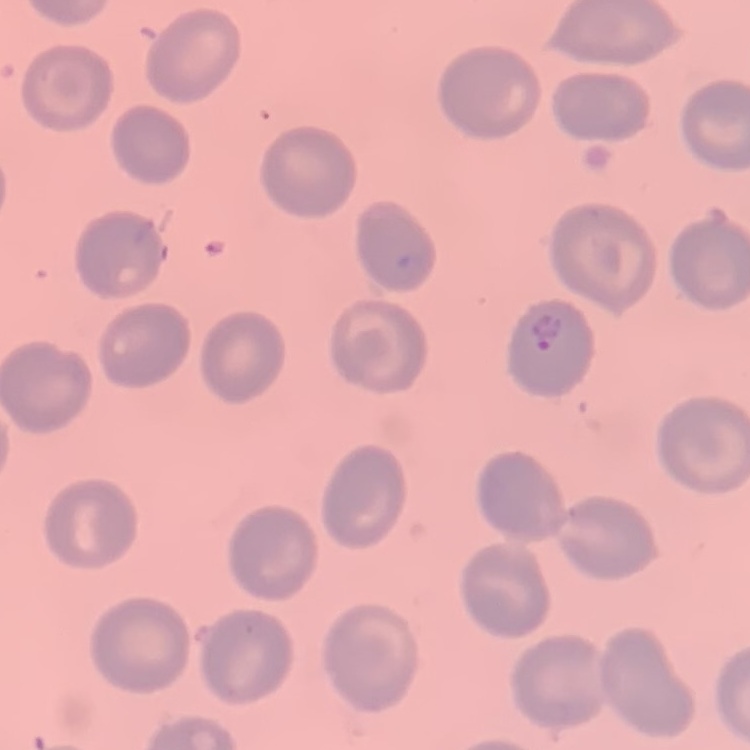
erythrocyte morphology = no rouleaux formation
stain = Field's or Giemsa
preparation = thin peripheral smear
image type = one tile cut from a larger photomicrograph